Give the extent of all Plasmodium ovale-infected red blood cells.
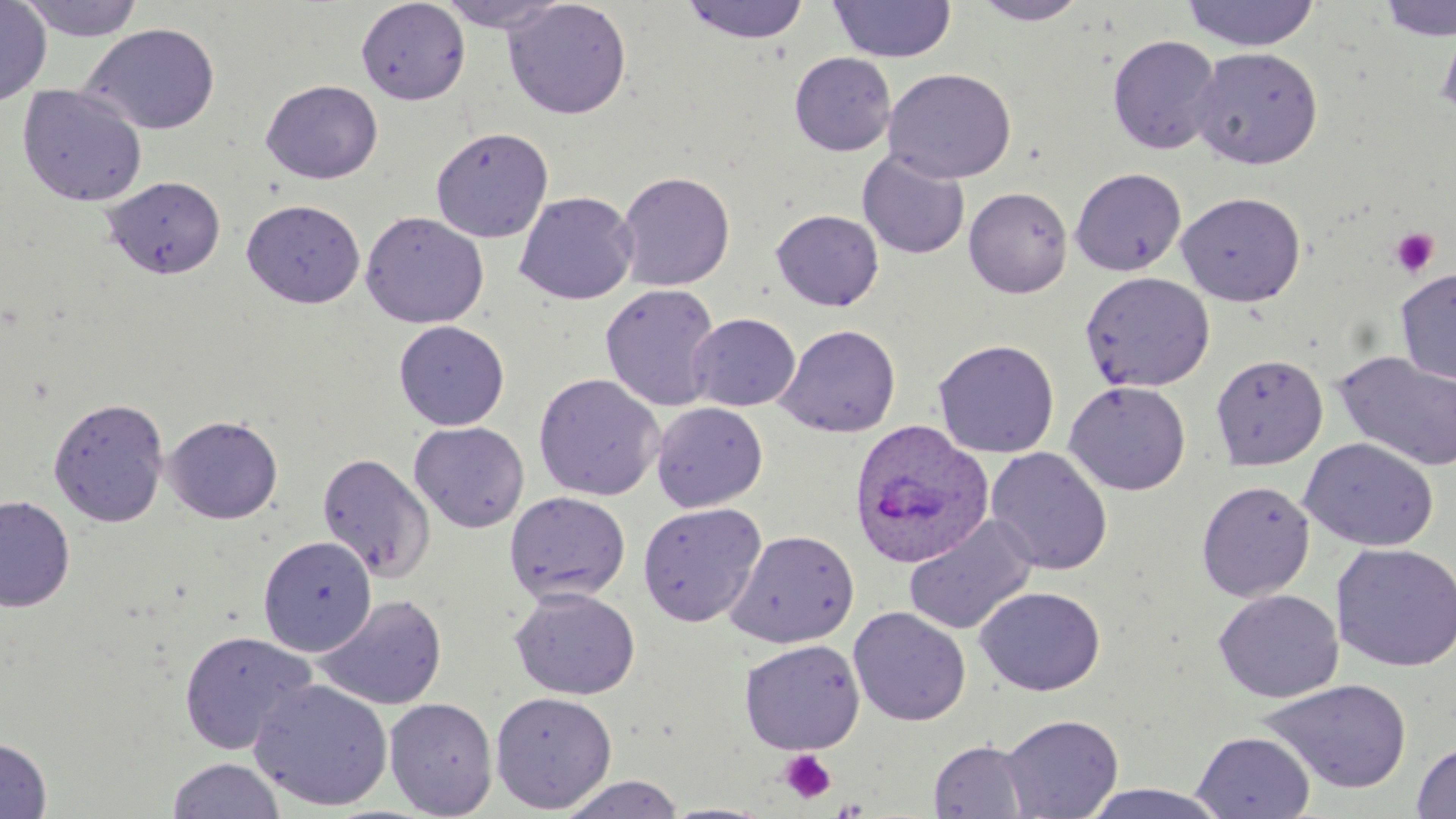
Approximate bounding boxes as named x1/y1/x2/y2 corners in pixels.
Plasmodium ovale-infected red blood cells: (x1=847, y1=418, x2=994, y2=568).

{
  "slide_level_diagnosis": "Plasmodium ovale",
  "magnification": "1000x",
  "preparation": "thin blood film",
  "stain": "May-Grünwald-Giemsa",
  "platelet_locations": "approximate bounding boxes as named x1/y1/x2/y2 corners in pixels: (x1=1389, y1=227, x2=1440, y2=279), (x1=778, y1=749, x2=837, y2=804)",
  "field_of_view": "single",
  "uninfected_red_blood_cell_locations": "approximate bounding boxes as named x1/y1/x2/y2 corners in pixels: (x1=0, y1=0, x2=51, y2=108), (x1=15, y1=0, x2=149, y2=42), (x1=355, y1=0, x2=471, y2=105), (x1=436, y1=0, x2=569, y2=33), (x1=502, y1=0, x2=632, y2=120), (x1=680, y1=0, x2=811, y2=46), (x1=828, y1=0, x2=956, y2=63), (x1=1181, y1=0, x2=1320, y2=52), (x1=1375, y1=0, x2=1456, y2=42), (x1=970, y1=1, x2=1090, y2=26), (x1=1436, y1=18, x2=1456, y2=126), (x1=82, y1=23, x2=221, y2=136), (x1=1106, y1=34, x2=1222, y2=155), (x1=1191, y1=46, x2=1323, y2=169), (x1=789, y1=52, x2=896, y2=156), (x1=883, y1=67, x2=1017, y2=184), (x1=261, y1=80, x2=383, y2=184), (x1=17, y1=84, x2=148, y2=207), (x1=430, y1=126, x2=553, y2=243), (x1=857, y1=150, x2=970, y2=259), (x1=1070, y1=167, x2=1187, y2=276), (x1=615, y1=170, x2=736, y2=291), (x1=102, y1=176, x2=226, y2=279), (x1=963, y1=186, x2=1073, y2=297), (x1=514, y1=191, x2=639, y2=305), (x1=1176, y1=191, x2=1306, y2=306), (x1=241, y1=198, x2=365, y2=308), (x1=771, y1=209, x2=884, y2=311), (x1=360, y1=211, x2=489, y2=329), (x1=1395, y1=267, x2=1456, y2=384), (x1=1079, y1=271, x2=1215, y2=392), (x1=600, y1=283, x2=722, y2=412), (x1=687, y1=313, x2=800, y2=412), (x1=393, y1=320, x2=510, y2=431), (x1=775, y1=323, x2=902, y2=437), (x1=932, y1=338, x2=1060, y2=458), (x1=1334, y1=350, x2=1456, y2=472), (x1=1210, y1=354, x2=1328, y2=470), (x1=533, y1=372, x2=665, y2=501), (x1=1064, y1=380, x2=1191, y2=495), (x1=48, y1=396, x2=170, y2=527), (x1=651, y1=401, x2=768, y2=512), (x1=164, y1=414, x2=284, y2=524), (x1=409, y1=421, x2=530, y2=533), (x1=1299, y1=437, x2=1439, y2=552), (x1=985, y1=446, x2=1113, y2=576), (x1=317, y1=452, x2=435, y2=582), (x1=1196, y1=480, x2=1315, y2=601), (x1=504, y1=491, x2=631, y2=606), (x1=0, y1=495, x2=75, y2=612), (x1=637, y1=502, x2=767, y2=627), (x1=904, y1=514, x2=1038, y2=635), (x1=725, y1=529, x2=859, y2=648), (x1=258, y1=535, x2=377, y2=655), (x1=1330, y1=543, x2=1456, y2=672), (x1=974, y1=585, x2=1106, y2=696), (x1=509, y1=587, x2=640, y2=700), (x1=1213, y1=589, x2=1343, y2=703), (x1=314, y1=594, x2=448, y2=710), (x1=848, y1=606, x2=971, y2=726), (x1=179, y1=630, x2=318, y2=756), (x1=738, y1=638, x2=865, y2=754), (x1=250, y1=677, x2=393, y2=811), (x1=1257, y1=679, x2=1413, y2=795), (x1=489, y1=690, x2=618, y2=812), (x1=384, y1=697, x2=498, y2=817), (x1=1000, y1=714, x2=1123, y2=818), (x1=1192, y1=731, x2=1315, y2=818), (x1=0, y1=737, x2=52, y2=818), (x1=929, y1=739, x2=1033, y2=818), (x1=1411, y1=740, x2=1456, y2=819), (x1=167, y1=758, x2=286, y2=819), (x1=556, y1=774, x2=687, y2=818), (x1=1078, y1=783, x2=1235, y2=818), (x1=661, y1=801, x2=778, y2=819)",
  "modality": "light microscopy",
  "image_size": "1456×819 pixels"
}